Name the parasite shown.
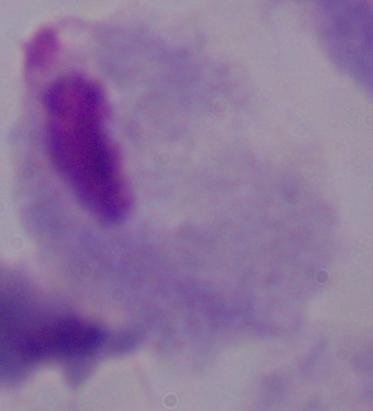
This is a trichomonad.

Summary:
  - Modality: photomicrograph
  - Magnification: 1000x